Identify the parasite.
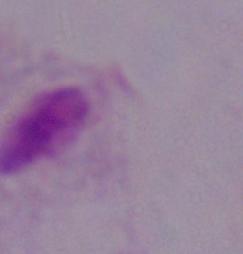

A trichomonad.

Summary:
  - Magnification: 1000x
  - Modality: micrograph